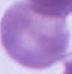

Micrograph. A red blood cell is shown. 1000x magnification.